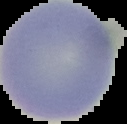

From a thin blood smear. Segmented cell region on a black background. Result: no malaria parasites detected. Image is 127×124 pixels.